State the preparation type.
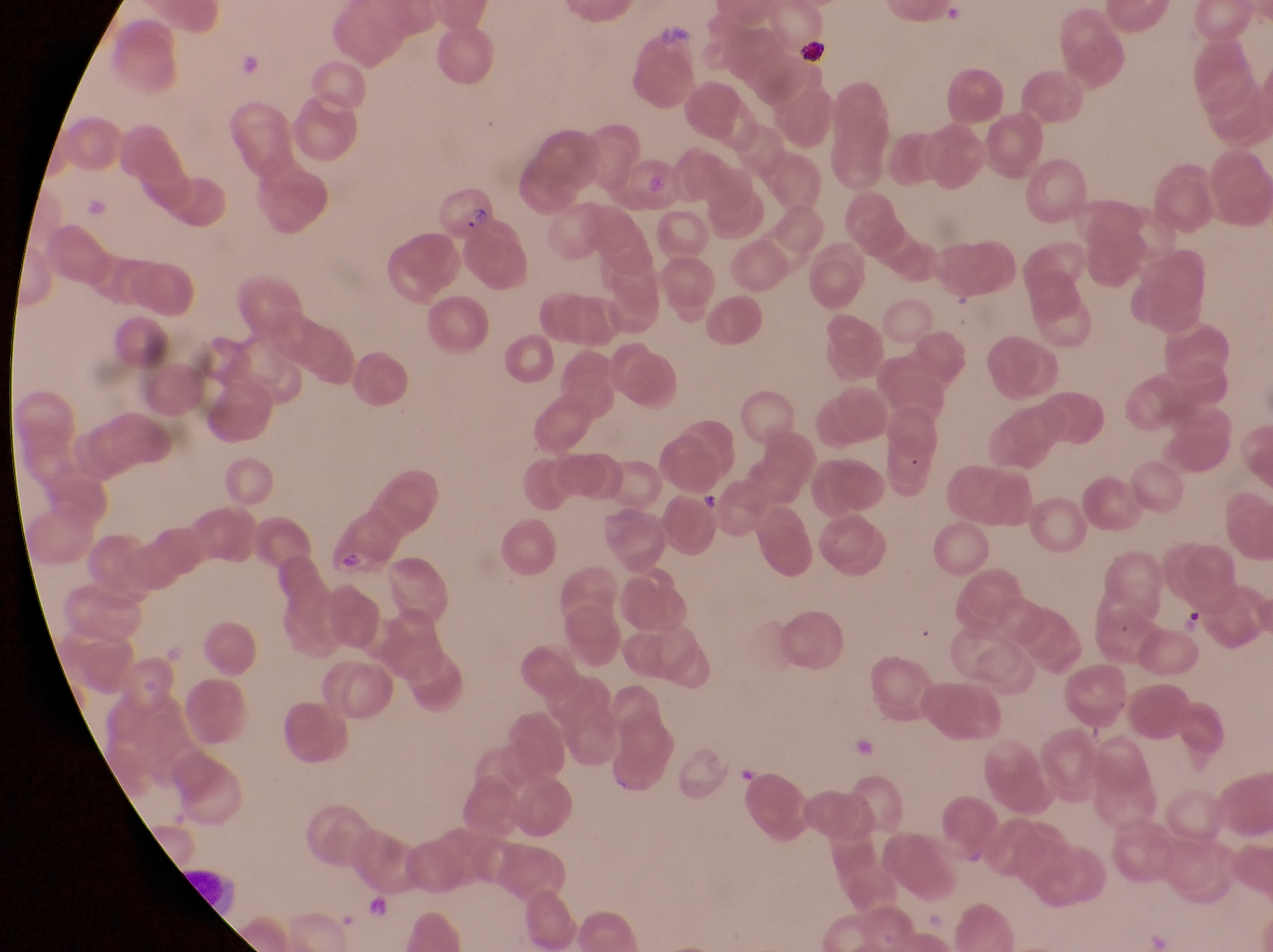

Thin blood smear.

Approximate bounding boxes as (left, top, right, bottom) in pixels.
Summary:
  - Artifact (platelet-like body, stain precipitate, or debris) locations: (335, 549, 368, 584)
  - Parasitised red blood cell locations: (427, 174, 501, 244)
  - Trophozoite locations: (692, 485, 725, 513)
  - Country: Uganda
  - Magnification: 1000x
  - Capture: smartphone photograph through the eyepiece of an Olympus CX-23 microscope
  - Field of view: single
  - Image size: 1273×952 pixels